Identify the parasite.
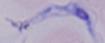

This is a trypanosome.

Summary:
  - Magnification: 1000x
  - Modality: micrograph